Assess the morphology of the erythrocytes.
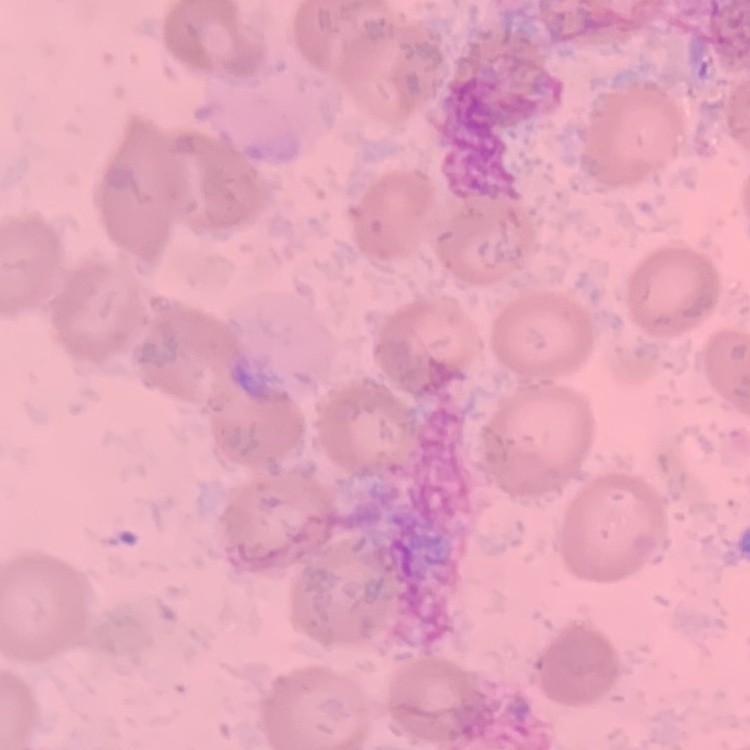
They show no rouleaux formation.

Square crop of a larger photomicrograph. Field's or Giemsa stain. Thin peripheral smear.